Assess for malaria.
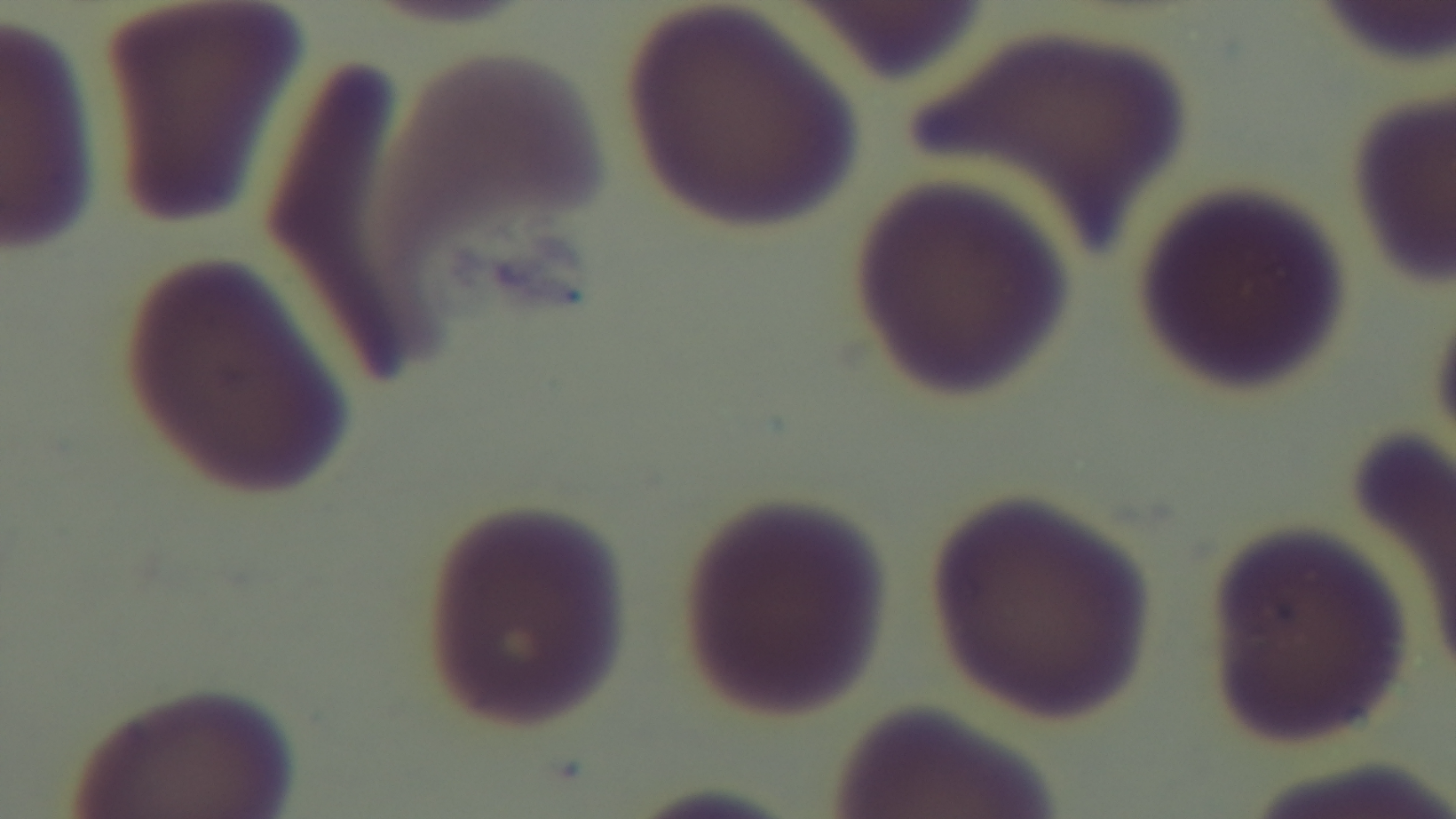
It is uninfected.

Summary:
  - Stain: Giemsa
  - Field of view: one from the slide
  - Preparation: thin
  - Capture: mounted 4K digital camera
  - Modality: light microscopy
  - Objective: 100x oil immersion